Give the location of every parasitized red blood cell.
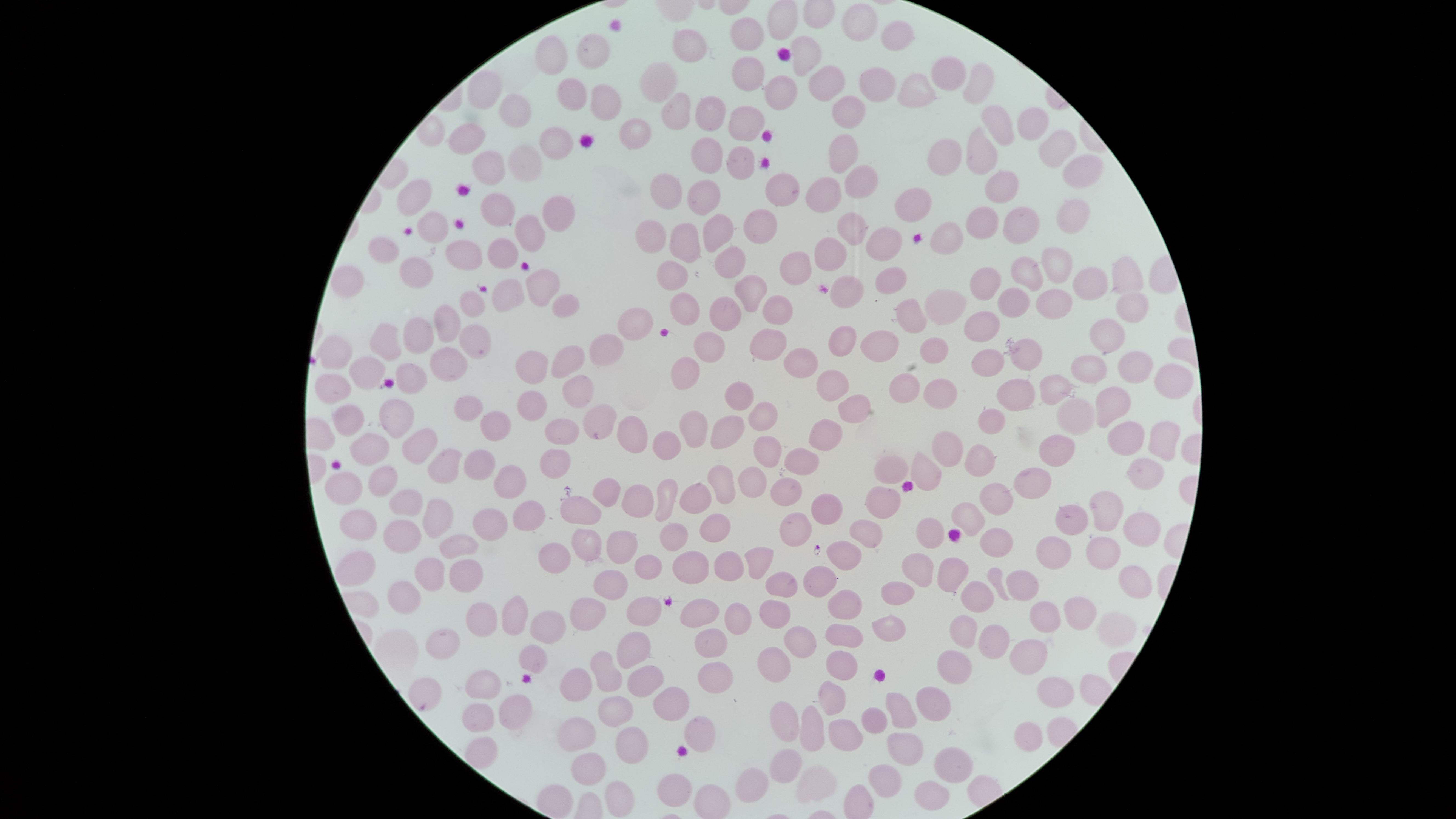
No parasitized red blood cells identified.

Approximate marker points as (x, y) in pixels.
Summary:
  - Uninfected red blood cells: (857, 21), (749, 32), (891, 36), (555, 47), (677, 51), (807, 53), (592, 63), (743, 73), (945, 73), (978, 79), (818, 80), (868, 81), (660, 82), (917, 86), (778, 89), (483, 90), (571, 92), (601, 105), (513, 107), (670, 108), (844, 112), (712, 113), (740, 119), (1028, 122), (632, 125), (996, 125), (465, 132), (548, 141), (1049, 143), (840, 147), (705, 150), (980, 150), (947, 151), (731, 159), (516, 164), (483, 165), (1075, 165), (856, 176), (1005, 185), (784, 189), (671, 193), (821, 193), (412, 194), (702, 195), (919, 199), (497, 208), (544, 210), (1066, 215), (974, 219), (431, 220), (1014, 220), (713, 228), (765, 228), (527, 230), (654, 230), (850, 231), (946, 233), (685, 241), (877, 244), (378, 247), (505, 249), (829, 253), (458, 255), (722, 260), (797, 261), (1061, 261), (1031, 267), (408, 270), (673, 270), (1123, 276), (888, 278), (986, 278), (342, 279), (1088, 280), (535, 283), (749, 288), (846, 291), (1008, 291), (1050, 293), (503, 298), (939, 298), (468, 302), (1122, 302), (560, 307), (685, 308), (777, 308), (913, 312), (723, 315), (444, 323), (635, 325), (974, 325), (417, 331), (474, 333), (841, 333), (1106, 335), (876, 340), (764, 341), (376, 343), (706, 343), (608, 349), (935, 349), (334, 354), (1025, 355), (799, 357), (986, 357), (569, 360), (1091, 362), (448, 363), (528, 367), (1141, 369), (364, 372), (683, 372), (1160, 380), (826, 381), (1056, 381), (903, 383), (325, 388), (577, 388), (941, 389), (1020, 391), (736, 396), (532, 398), (1113, 401), (850, 403), (471, 405), (1066, 409), (759, 411), (343, 417), (497, 418), (990, 418), (386, 419), (594, 419), (690, 423), (553, 429), (723, 431), (827, 431), (1129, 433), (630, 434), (668, 438), (1158, 438), (423, 441), (1055, 444), (950, 445), (767, 449), (369, 450), (970, 459), (795, 460), (545, 461), (447, 464), (481, 466), (890, 466), (923, 471), (513, 473), (1140, 475), (376, 482), (746, 482), (1042, 483), (718, 484), (606, 488), (345, 489), (781, 492), (630, 494), (662, 495), (698, 496), (884, 499), (407, 502), (1000, 502), (828, 508), (583, 509), (1079, 512), (518, 513), (1106, 513), (965, 518), (486, 519), (427, 521), (704, 522), (367, 524), (672, 524), (796, 524), (1132, 524), (868, 525), (400, 529), (934, 530), (614, 540), (452, 541), (583, 543), (1001, 544), (1101, 547), (757, 553), (1065, 553), (555, 556), (723, 556), (650, 557), (352, 558), (846, 558), (689, 564), (915, 566), (459, 568), (424, 572), (945, 574), (819, 578), (775, 581), (1125, 581), (606, 585), (1029, 585), (893, 591), (403, 595), (970, 595), (647, 606), (839, 606), (773, 610), (1073, 610), (699, 612), (578, 613), (507, 614), (1045, 615), (484, 619), (734, 619), (539, 627), (1114, 629), (958, 630), (883, 631), (450, 634), (839, 636), (801, 638), (996, 638), (708, 640), (633, 644), (1031, 657), (840, 661), (527, 663), (775, 664), (959, 664), (608, 668), (712, 677), (483, 679), (640, 683), (570, 684), (1045, 688), (424, 693), (837, 695), (672, 698), (929, 699), (503, 704), (897, 705), (614, 708), (475, 715), (779, 719), (872, 720), (802, 723), (699, 729), (844, 736), (1021, 739), (568, 745), (904, 745), (477, 746), (631, 749), (777, 756), (941, 762), (587, 767), (880, 777), (815, 778), (679, 780), (754, 783), (922, 789), (618, 794)
  - Preparation: thin blood smear
  - Stain: Giemsa
  - Image size: 1456×819 pixels
  - Field of view: single
  - Visible region: circular
  - Capture: smartphone photograph through the microscope eyepiece